Locate and identify every blood parasite.
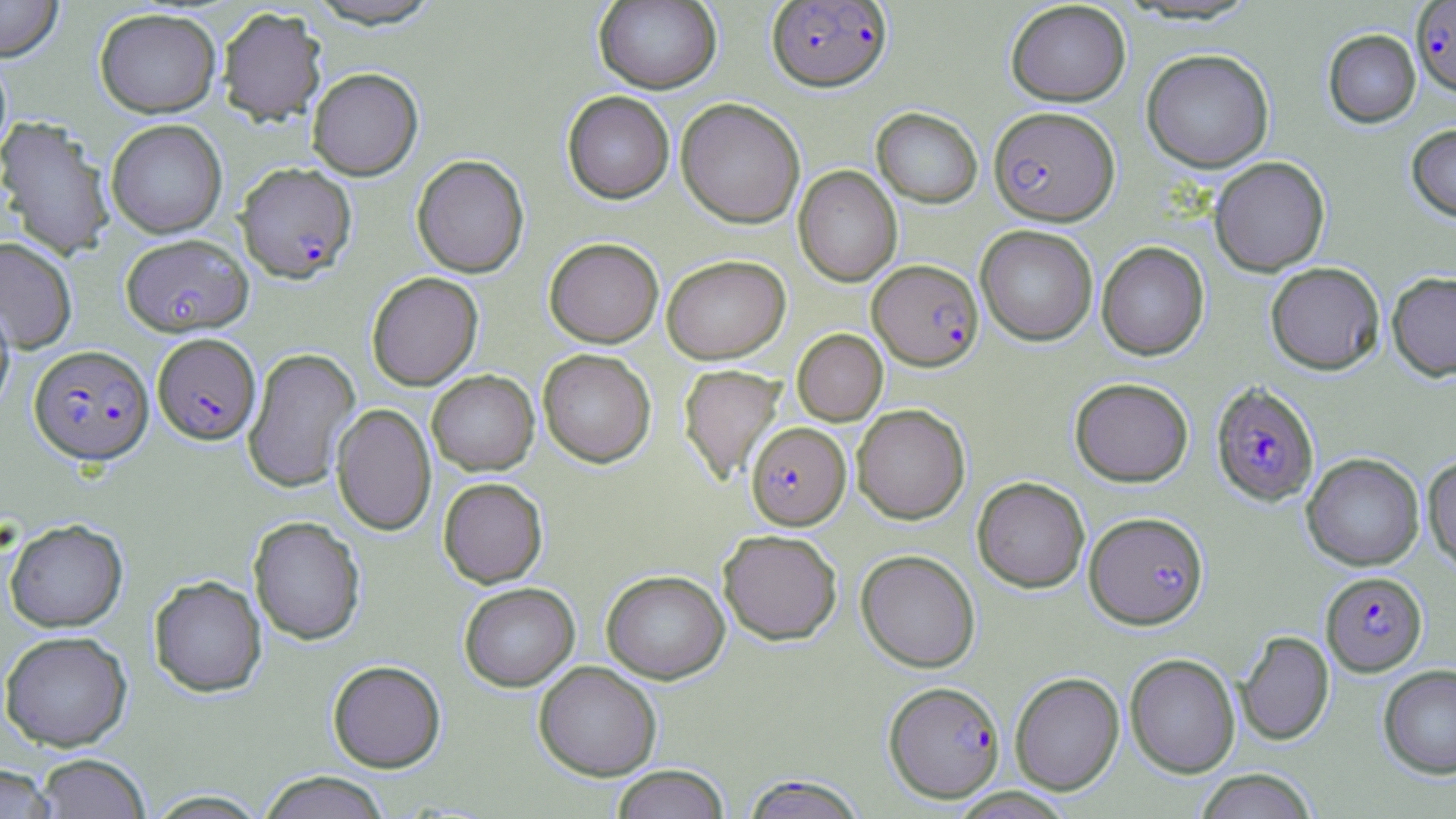

Approximate bounding boxes as (x1, y1, x2, y2) in pixels.
Plasmodium falciparum-infected red blood cells: (767, 0, 891, 91), (1410, 1, 1456, 96), (988, 106, 1119, 225), (236, 163, 357, 282), (121, 233, 252, 336), (868, 259, 983, 370), (152, 332, 261, 445), (29, 345, 153, 464), (1211, 382, 1319, 506), (746, 425, 850, 532), (1085, 511, 1208, 629), (1321, 571, 1427, 675), (884, 681, 1005, 802), (740, 775, 870, 818).
No Plasmodium ovale, Plasmodium malariae, Plasmodium vivax, Babesia divergens, or Trypanosoma brucei observed.

slide-level diagnosis = Plasmodium falciparum
magnification = 1000x
field of view = one of a larger specimen
image size = 1456×819 pixels
stain = May-Grünwald-Giemsa
uninfected red blood cell locations = approximate bounding boxes as (x1, y1, x2, y2) in pixels: (0, 0, 63, 61), (304, 0, 445, 29), (594, 1, 722, 93), (1005, 1, 1130, 106), (217, 7, 327, 126), (94, 8, 221, 118), (1323, 29, 1421, 127), (1142, 48, 1274, 172), (0, 51, 12, 163), (307, 67, 423, 180), (562, 91, 675, 203), (676, 98, 805, 228), (872, 107, 983, 208), (0, 115, 116, 261), (105, 119, 227, 238), (1406, 123, 1456, 223), (412, 154, 529, 277), (1209, 156, 1329, 276), (793, 166, 902, 286), (976, 224, 1098, 345), (0, 237, 77, 353), (544, 237, 664, 347), (1096, 241, 1210, 360), (662, 254, 790, 363), (1265, 262, 1385, 375), (366, 272, 483, 390), (1387, 272, 1456, 380), (0, 298, 15, 416), (792, 329, 888, 426), (243, 347, 361, 492), (538, 348, 656, 467), (679, 364, 786, 484), (427, 370, 539, 475), (1070, 377, 1194, 487), (332, 403, 436, 536), (852, 404, 970, 524), (1301, 453, 1424, 570), (1422, 454, 1456, 574), (438, 477, 548, 588), (972, 477, 1089, 593), (248, 515, 365, 645), (4, 518, 128, 632), (718, 529, 843, 645), (856, 549, 980, 672), (601, 569, 730, 684), (149, 574, 267, 697), (459, 582, 580, 691), (0, 630, 132, 751), (1236, 630, 1334, 745), (1125, 653, 1241, 777), (327, 660, 446, 772), (533, 661, 662, 781), (1378, 665, 1456, 779), (1010, 672, 1124, 795), (34, 753, 150, 818), (0, 763, 57, 818), (611, 765, 730, 819), (1193, 769, 1318, 819), (257, 771, 392, 819), (143, 789, 271, 818)
preparation = thin blood smear
modality = light microscopy